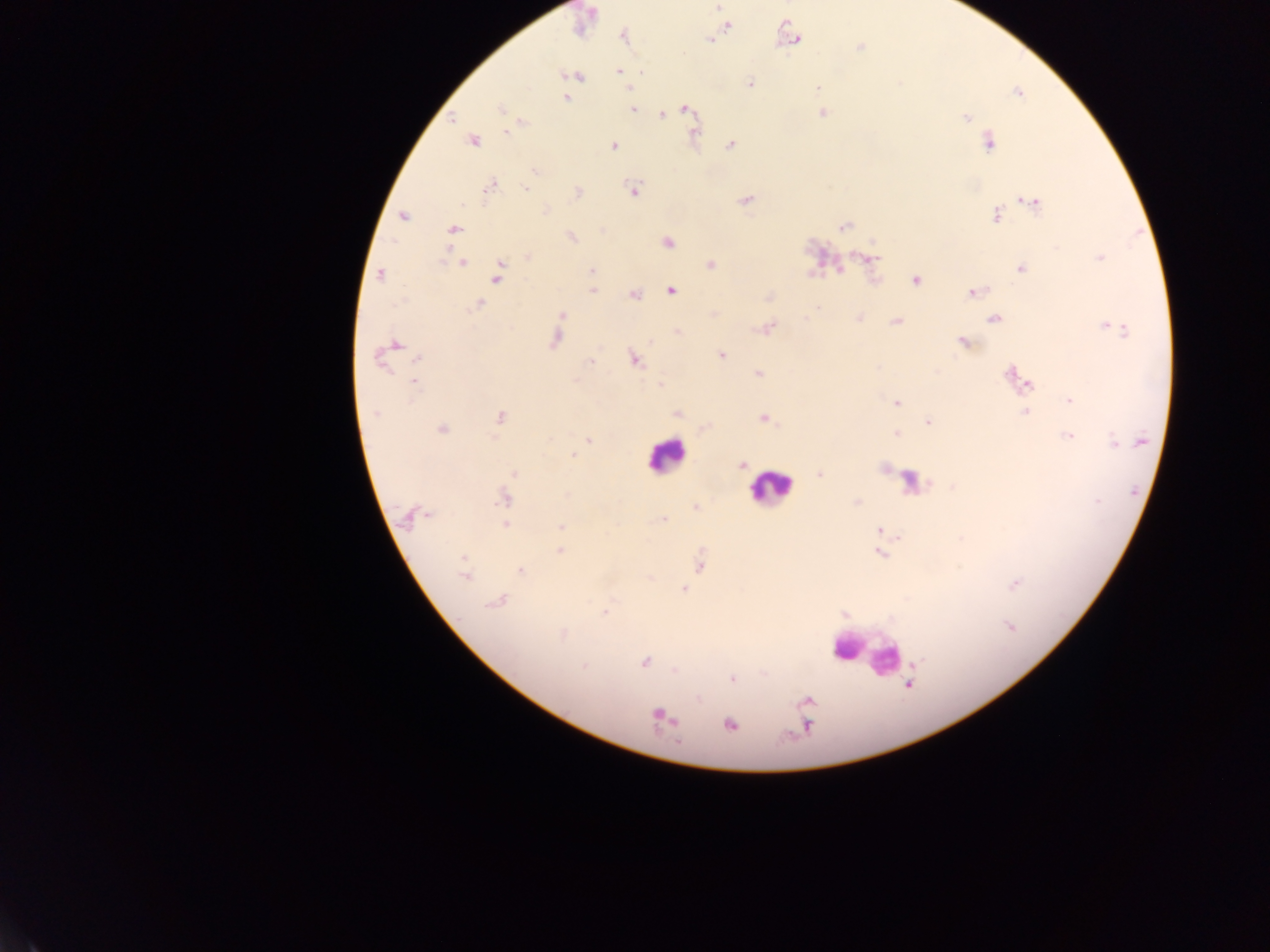

Approximate centers as [x, y] in pixels. Leukocyte locations: [665, 456], [769, 488], [863, 653]. Malaria parasite locations: [717, 7], [728, 25], [623, 35], [793, 38], [710, 40], [860, 47], [620, 72], [574, 75], [750, 83], [818, 88], [629, 89], [566, 97], [687, 109], [500, 110], [632, 110], [823, 113], [662, 115], [452, 118], [966, 118], [506, 132], [472, 142], [988, 142], [730, 145], [614, 146], [535, 172], [490, 187], [526, 189], [634, 191], [577, 193], [745, 200], [1033, 202], [996, 215], [403, 216], [843, 227], [453, 229], [572, 237], [668, 242], [528, 257], [868, 258], [1099, 258], [463, 262], [711, 264], [1021, 269], [591, 270], [498, 273], [380, 276], [916, 280], [592, 291], [670, 291], [973, 292], [634, 295], [479, 304], [562, 315], [805, 319], [859, 319], [994, 319], [896, 321], [767, 328], [1115, 330], [556, 339], [650, 342], [962, 343], [396, 344], [721, 354], [418, 357], [635, 359], [380, 361], [590, 362], [759, 374], [1013, 375], [1027, 382], [414, 383], [660, 385], [1070, 401], [897, 402], [1025, 412], [676, 413], [376, 414], [500, 417], [764, 419], [929, 422], [442, 429], [895, 434], [1068, 436], [589, 440], [1114, 442], [573, 455], [742, 465], [514, 474], [820, 474], [503, 499], [1098, 501], [857, 503], [695, 507], [426, 515], [663, 519], [505, 524], [561, 526], [879, 530], [560, 551], [880, 554], [463, 558], [700, 565], [521, 571], [465, 577], [1015, 583], [684, 589], [496, 602], [605, 612], [1011, 627], [563, 634], [918, 661], [645, 662], [583, 666], [675, 671], [733, 679], [908, 685], [807, 701], [661, 716], [730, 725], [807, 726]. Mobile-phone photograph taken through the microscope. Collected in Ghana. Thick blood smear. Image is 1270×952 pixels. One field of view.